Describe the morphology of the red blood cells.
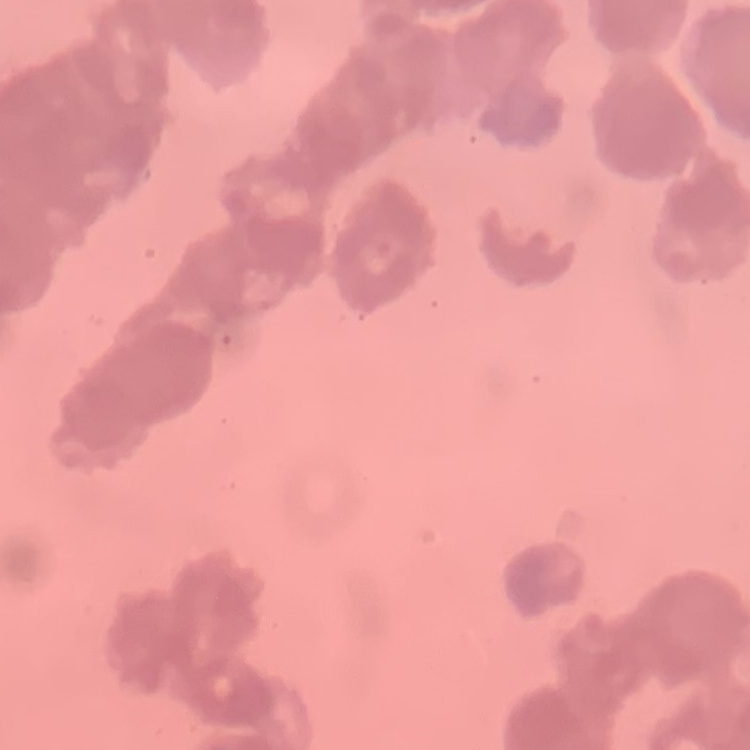
Rouleaux formation.

One tile cut from a larger photomicrograph. Thin blood smear. Stained with either Field's or Giemsa.